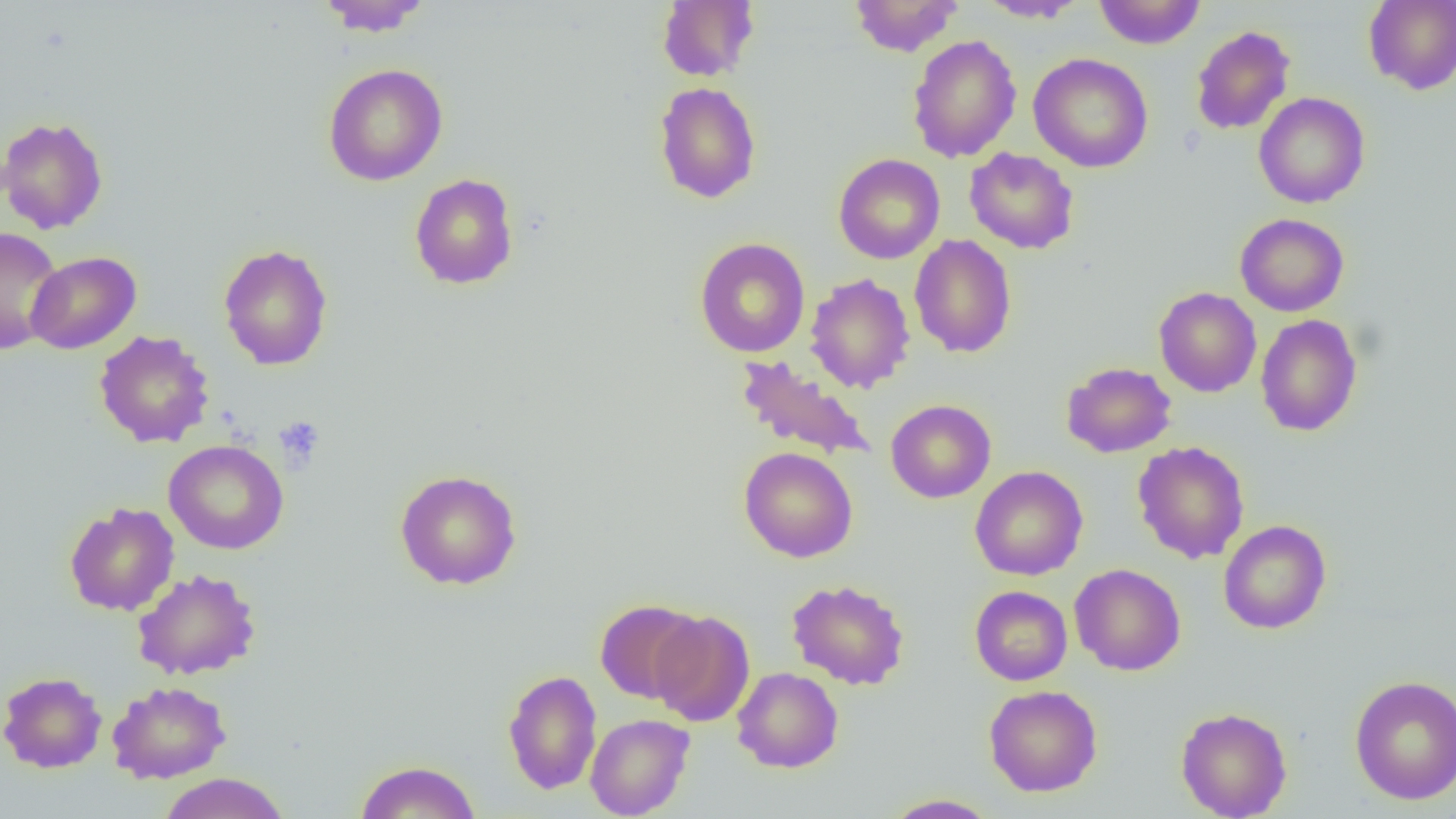
Summary:
  - Coordinate format: approximate bounding boxes as (x1,y1)-(x2,y2) corner pairs in pixels
  - Platelet locations: (274,415)-(325,471)
  - Uninfected red blood cell locations: (317,0)-(432,36), (657,0)-(759,82), (848,0)-(963,57), (977,0)-(1089,23), (1093,0)-(1206,49), (1363,0)-(1456,95), (1190,25)-(1296,136), (906,34)-(1022,163), (1028,52)-(1154,173), (323,63)-(448,186), (654,81)-(761,204), (1253,92)-(1369,208), (0,116)-(109,235), (964,148)-(1080,254), (833,153)-(945,264), (409,173)-(519,290), (1235,213)-(1349,316), (0,226)-(64,355), (909,234)-(1017,358), (695,237)-(810,358), (218,243)-(333,371), (26,251)-(141,354), (805,273)-(916,393), (1153,287)-(1262,397), (1255,314)-(1363,437), (93,330)-(215,448), (734,355)-(877,463), (1061,361)-(1176,458), (885,399)-(996,503), (164,439)-(289,555), (1133,440)-(1249,564), (739,447)-(858,562), (970,465)-(1088,581), (394,469)-(522,590), (64,502)-(180,616), (1218,520)-(1331,634), (1069,563)-(1186,676), (132,568)-(261,680), (786,579)-(910,690), (969,585)-(1072,685), (594,598)-(705,703), (649,610)-(755,727), (732,667)-(844,773), (502,669)-(602,794), (0,672)-(107,773), (1349,674)-(1456,805), (107,681)-(232,784), (983,684)-(1102,797), (1176,706)-(1292,819), (585,713)-(695,819), (355,760)-(482,819), (158,772)-(290,819), (882,794)-(1000,818)
  - Slide-level diagnosis: no evidence of blood parasites
  - Field of view: one of a larger specimen
  - Magnification: 1000x
  - Image size: 1456×819 pixels
  - Modality: light microscopy
  - Preparation: thin blood smear